State which parasite is depicted.
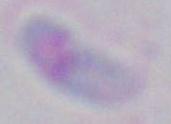

This is Toxoplasma gondii.

Summary:
  - Magnification: 1000x
  - Modality: photomicrograph